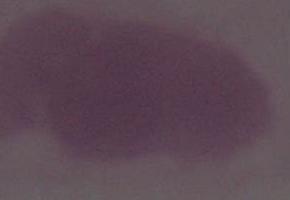 Photomicrograph. An erythrocyte is shown. Captured at 1000x magnification.